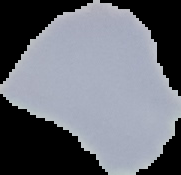

Result: no malaria parasites detected. Image is 181×175 pixels. From a thin blood film. The area outside the segmented cell region is set to black.